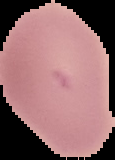

Summary:
  - Image size: 115×160 pixels
  - Preparation: thin blood smear
  - Image type: cell region segmented out of the field of view; surrounding area masked to black
  - Malaria status: uninfected